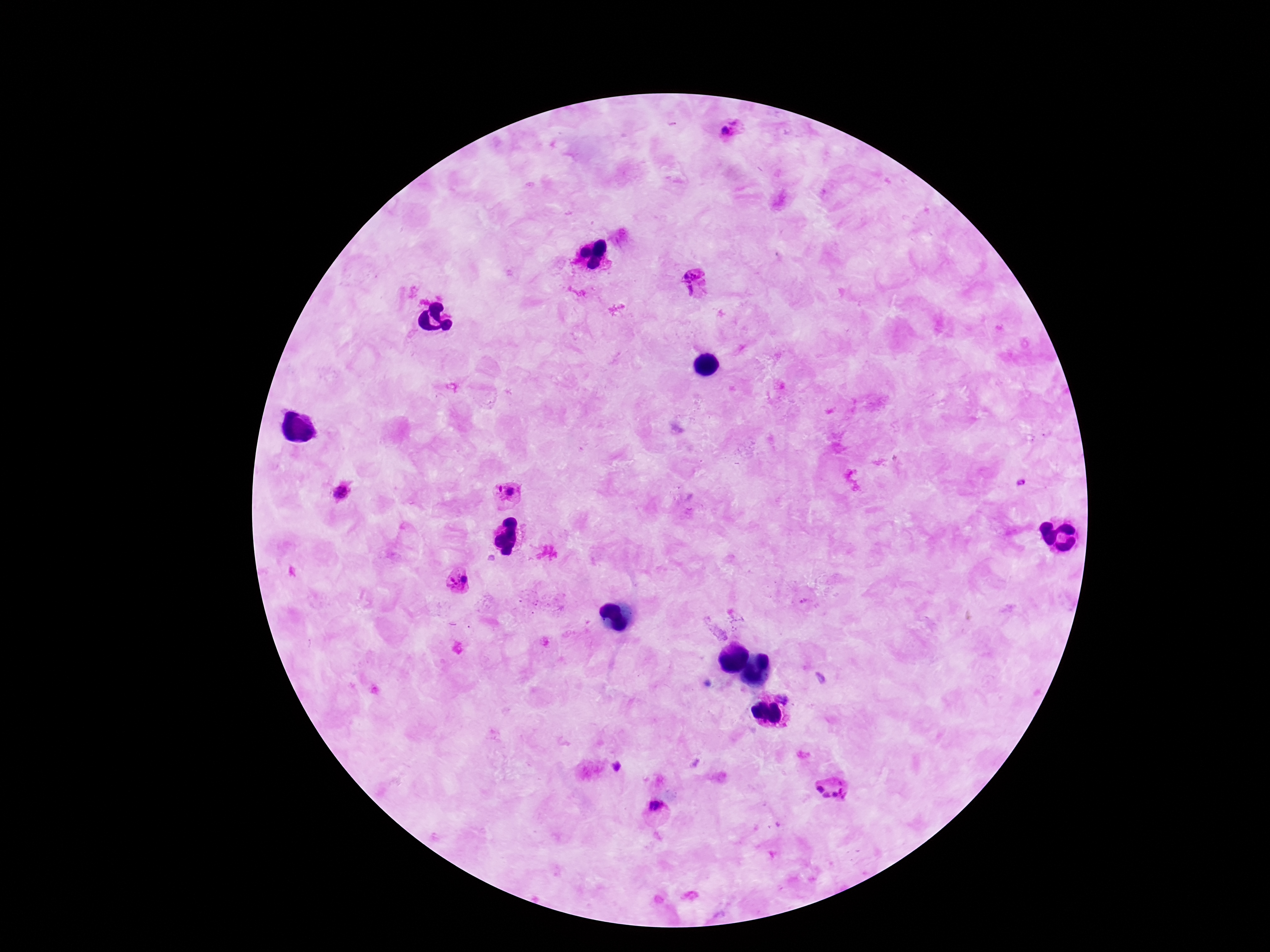

Approximate object centers, in pixels from the top-left corner. Plasmodium parasite locations: (x=732, y=134), (x=697, y=284), (x=1022, y=484), (x=497, y=489), (x=512, y=492), (x=339, y=493), (x=465, y=578), (x=453, y=582), (x=783, y=698), (x=615, y=767), (x=833, y=790), (x=655, y=806). Image is 1270×952 pixels. Thick peripheral-blood smear. Patient malaria status: infected. Giemsa stain. One field from this slide. Photographed through the microscope eyepiece with a smartphone camera. 100x magnification.